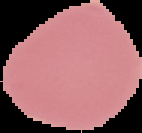

result: negative for Plasmodium parasites
image_type: segmented cell region with the area outside set to black
preparation: thin blood smear
image_size: 142×133 pixels